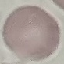 Result: negative for malaria parasites. Giemsa-stained preparation. Cell patch, automatically extracted from a larger field of view and resized to 64 × 64 pixels. Photographed with a smartphone camera at the microscope eyepiece. Thin blood film.